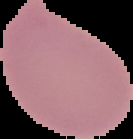
Segmented cell region on a black background. Image is 133×139 pixels. From a thin blood film. Malaria status: uninfected.